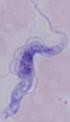
Summary:
  - Magnification: 1000x
  - Modality: photomicrograph
  - Identification: trypanosome